Describe the morphology of the erythrocytes.
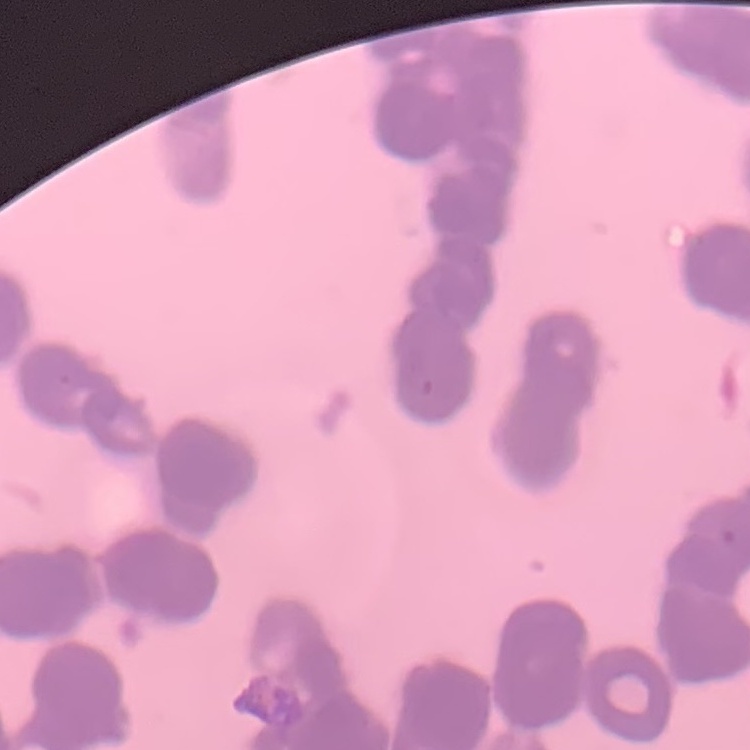
They show rouleaux formation.

image type = one tile cut from a larger photomicrograph
preparation = thin blood film
stain = Field's or Giemsa